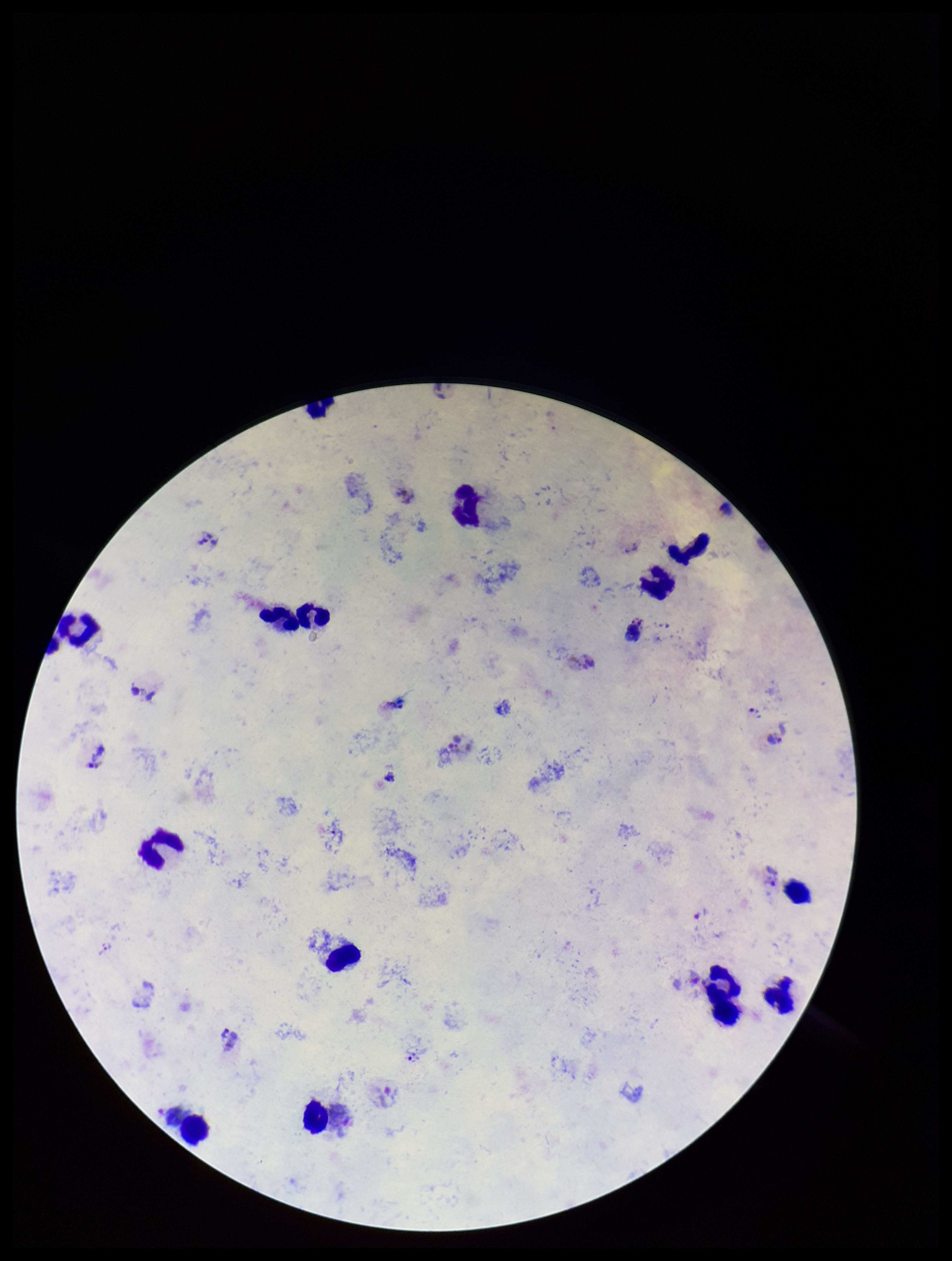

{
  "plasmodium_parasites": "identified",
  "species_reported_for_this_patient": "Plasmodium vivax",
  "parasite_count": 6,
  "patient_malaria_status": "infected",
  "capture": "smartphone photograph through the microscope eyepiece",
  "leukocyte_count": 14,
  "preparation": "thick",
  "stain": "Giemsa",
  "image_size": "952×1261 pixels",
  "field_of_view": "single"
}